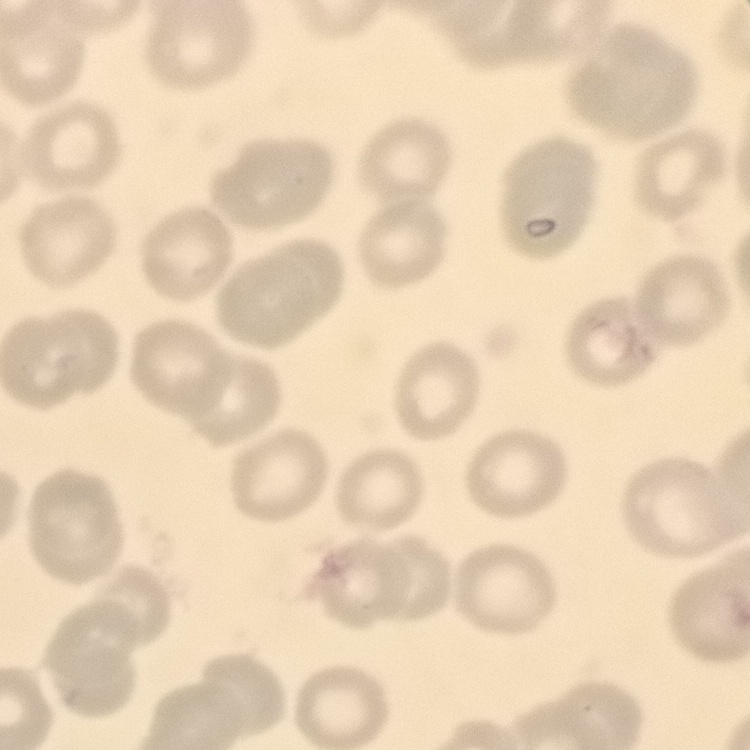
Summary:
  - Erythrocyte morphology: no rouleaux formation
  - Stain: Field's or Giemsa
  - Image type: one tile cut from a larger photomicrograph
  - Preparation: thin blood smear